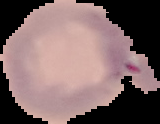
preparation = thin blood smear
malaria status = uninfected
image size = 160×124 pixels
image type = cell region segmented out of the field of view; surrounding area masked to black